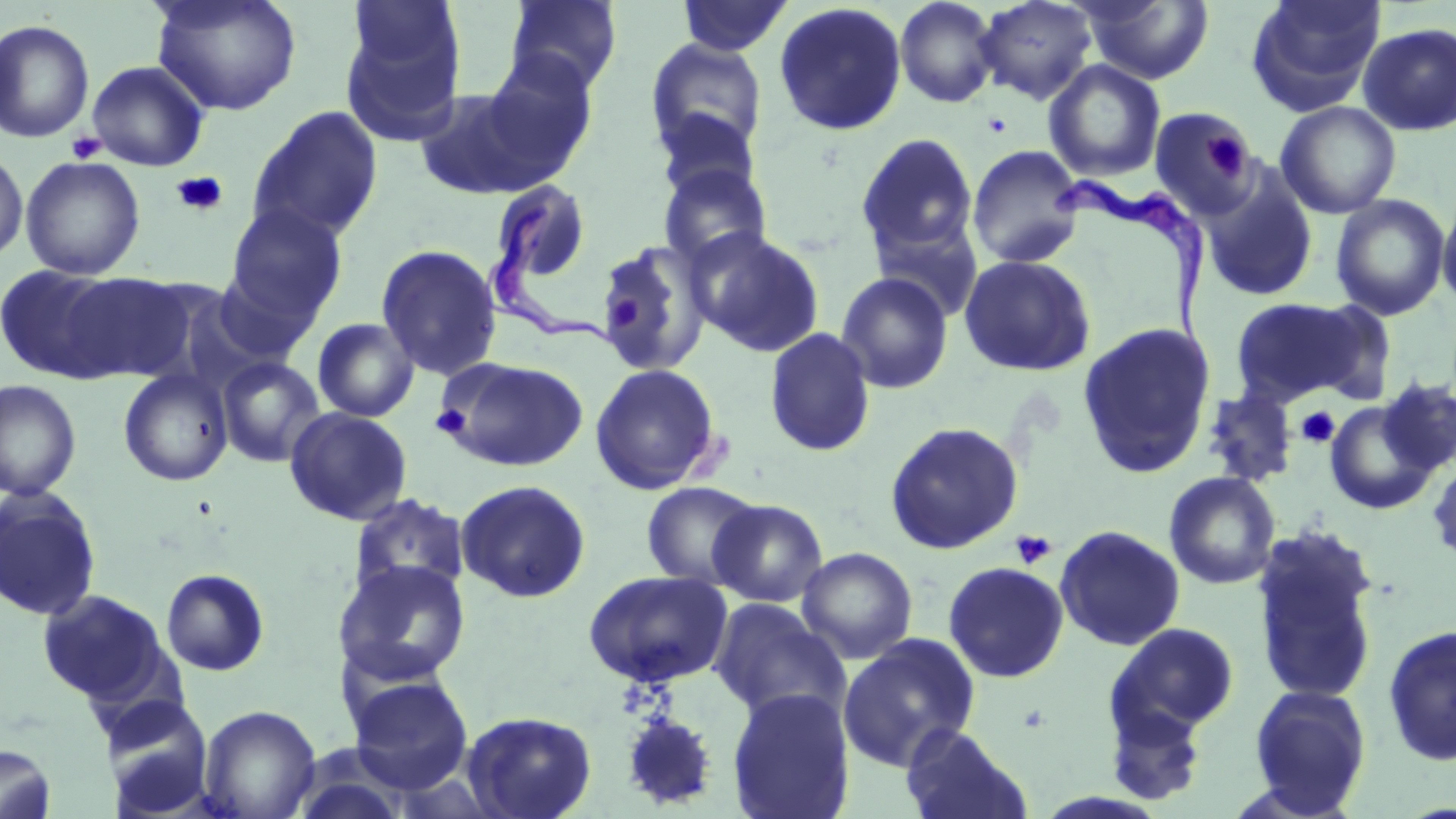

Approximate bounding boxes as [x1, y1, x2, y2] in pixels. Uninfected red blood cell locations: [149, 0, 302, 116], [502, 0, 624, 97], [676, 0, 793, 57], [894, 0, 1000, 109], [974, 0, 1098, 106], [1079, 0, 1215, 85], [1246, 0, 1386, 113], [773, 3, 908, 136], [340, 5, 468, 144], [0, 19, 95, 143], [1358, 23, 1456, 136], [644, 38, 769, 161], [471, 55, 599, 180], [1043, 59, 1166, 182], [86, 60, 211, 171], [415, 81, 572, 202], [1275, 101, 1402, 219], [247, 106, 384, 243], [1149, 107, 1260, 219], [653, 110, 763, 206], [856, 133, 978, 261], [966, 144, 1086, 269], [0, 149, 29, 263], [20, 155, 146, 280], [658, 163, 772, 269], [1202, 177, 1318, 302], [488, 179, 592, 289], [1330, 194, 1451, 321], [1438, 195, 1456, 311], [224, 204, 346, 324], [869, 213, 985, 323], [690, 229, 826, 357], [598, 241, 712, 376], [375, 244, 503, 380], [958, 253, 1097, 377], [0, 264, 130, 383], [207, 267, 324, 366], [55, 271, 197, 381], [836, 271, 954, 394], [1231, 297, 1359, 408], [1301, 301, 1400, 407], [312, 318, 420, 422], [1076, 322, 1215, 479], [764, 327, 876, 457], [216, 355, 326, 468], [437, 355, 587, 473], [589, 363, 721, 494], [118, 369, 233, 486], [1376, 377, 1456, 477], [0, 380, 82, 501], [1201, 388, 1298, 486], [1324, 399, 1439, 515], [284, 407, 413, 525], [884, 421, 1024, 555], [1427, 454, 1456, 568], [1164, 471, 1281, 589], [455, 480, 591, 603], [641, 481, 763, 590], [0, 487, 102, 622], [347, 493, 470, 603], [709, 498, 828, 607], [1054, 524, 1185, 651], [1250, 524, 1383, 705], [796, 546, 918, 664], [334, 560, 472, 687], [942, 561, 1069, 683], [161, 568, 270, 676], [582, 569, 733, 688], [36, 589, 172, 709], [709, 599, 850, 724], [1105, 622, 1240, 743], [1381, 623, 1456, 768], [838, 633, 981, 770], [345, 673, 474, 794], [1246, 684, 1372, 816], [728, 688, 854, 819], [1102, 692, 1210, 806], [103, 697, 215, 816], [197, 704, 321, 819], [461, 710, 596, 819], [898, 723, 1035, 819], [0, 744, 58, 819]. Platelet locations: [1204, 128, 1252, 179], [66, 132, 107, 164], [171, 171, 229, 218], [603, 294, 643, 336], [429, 404, 471, 440], [1296, 406, 1341, 448], [1010, 530, 1057, 570]. Trypanosoma brucei locations: [1054, 177, 1218, 376], [475, 203, 621, 352]. Slide-level diagnosis: Trypanosoma brucei. May-Grünwald-Giemsa-stained preparation. Image is 1456×819 pixels. Thin blood film. One field of a larger specimen. Captured at 1000x magnification. Light microscopy.